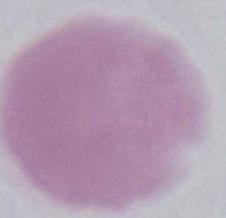
Summary:
  - Magnification: 1000x
  - Identification: erythrocyte
  - Modality: photomicrograph